Give the position of every Plasmodium parasite.
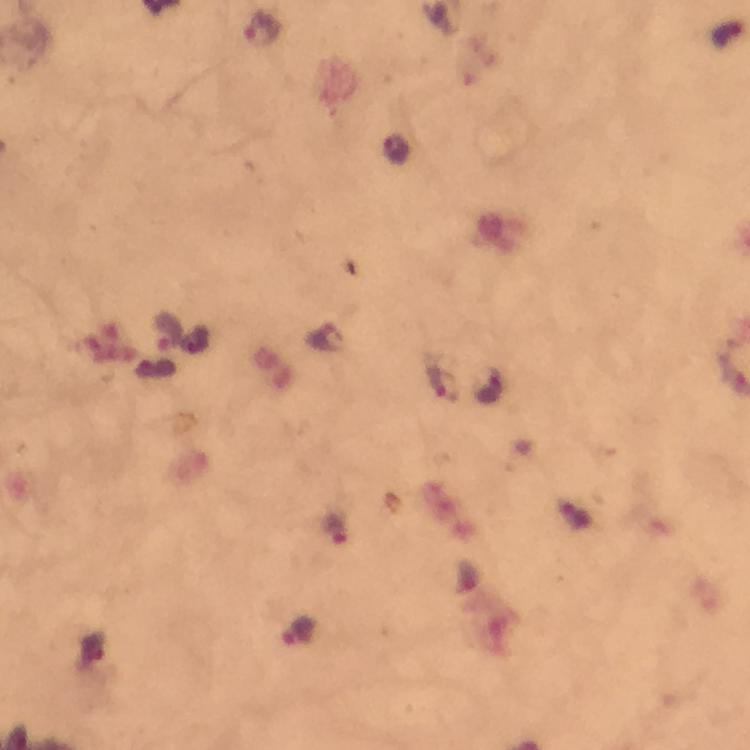
Approximate centers as {x, y} in pixels.
Plasmodium parasites: {264, 28}, {167, 331}, {440, 377}, {334, 528}.

Photographed with a smartphone mounted on the microscope. Immersion oil applied. Cropped region of a single field of view. Thick blood film. From a diagnostic examination for malaria. Image is 750×750 pixels. Giemsa-stained preparation. 100x magnification.